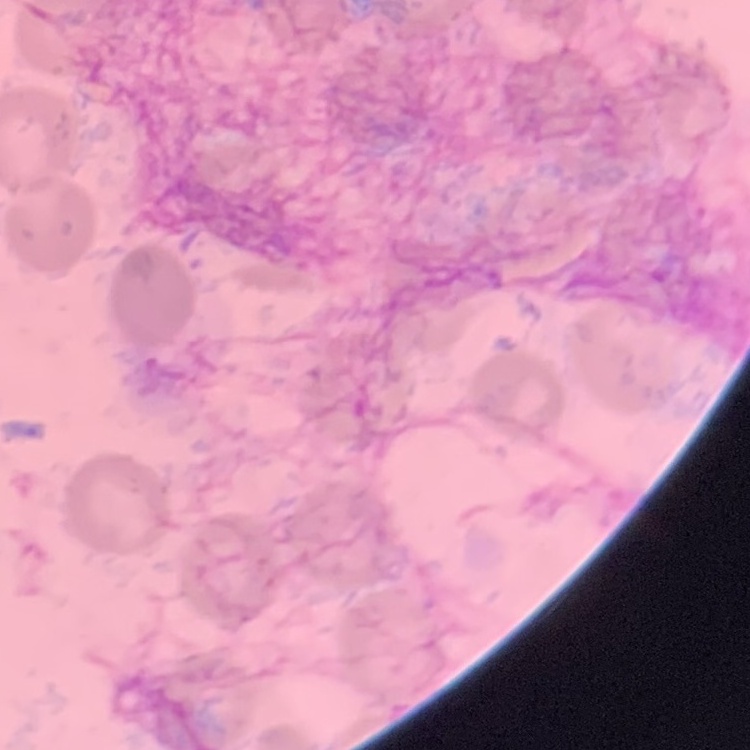 The erythrocytes show no rouleaux formation. Square crop of a larger photomicrograph. Stained with either Field's or Giemsa. Thin blood film.